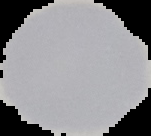

Summary:
  - Image type: cell region segmented out of the field of view; surrounding area masked to black
  - Image size: 151×136 pixels
  - Preparation: thin blood film
  - Result: no malaria parasites detected